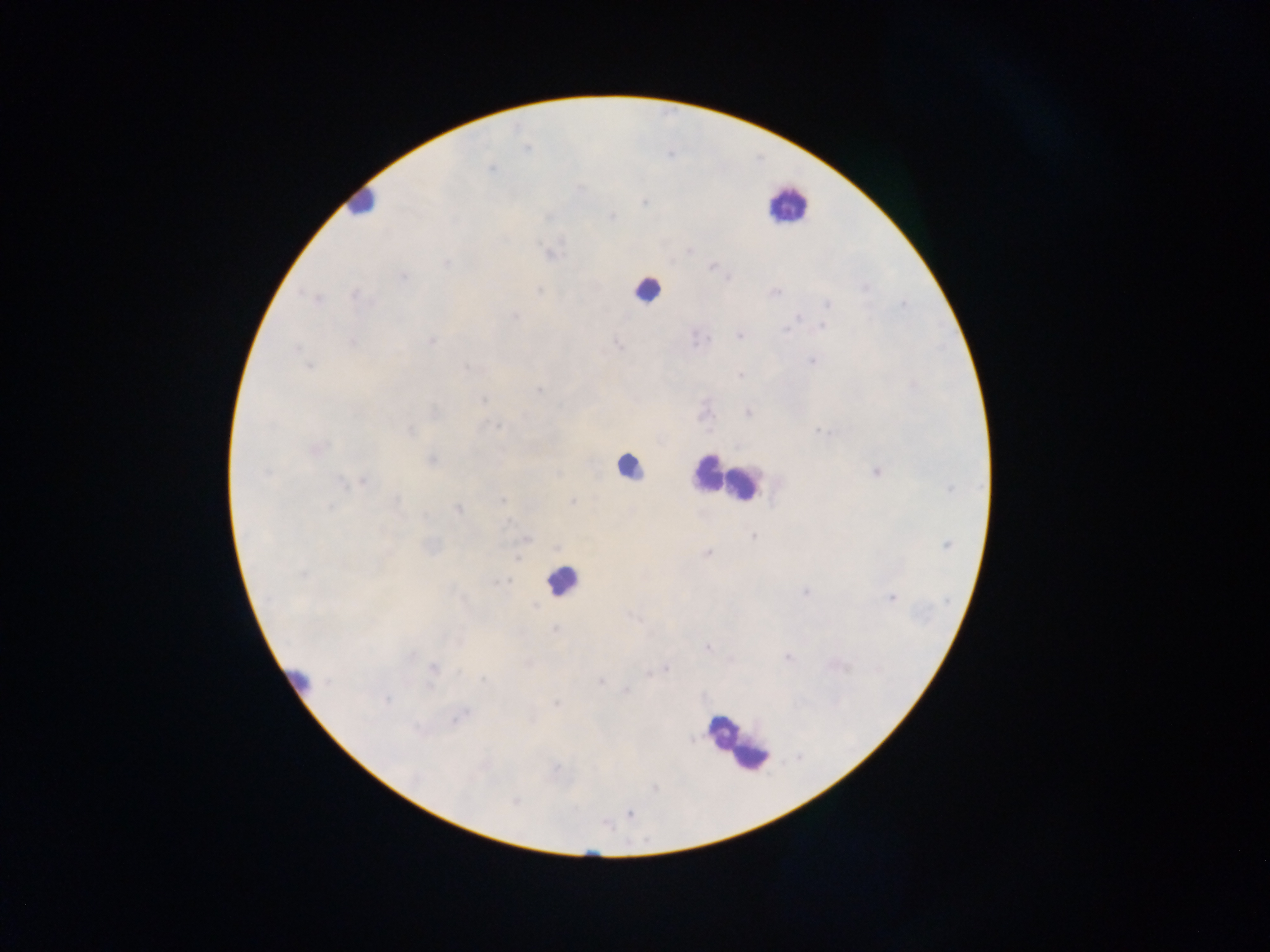
Approximate centers as [x, y] in pixels. Malaria parasite locations: [527, 149], [488, 169], [581, 187], [612, 216], [556, 248], [448, 264], [712, 267], [402, 277], [866, 288], [540, 290], [304, 292], [353, 294], [314, 298], [829, 304], [905, 305], [514, 316], [797, 318], [823, 325], [784, 329], [739, 336], [432, 341], [352, 343], [616, 343], [297, 348], [812, 361], [309, 366], [465, 367], [740, 375], [539, 389], [482, 399], [748, 412], [497, 426], [410, 430], [819, 431], [318, 449], [266, 472], [877, 473], [559, 474], [363, 481], [343, 482], [503, 500], [396, 501], [573, 501], [330, 507], [458, 509], [425, 515], [511, 523], [383, 531], [752, 536], [527, 539], [947, 544], [706, 554], [519, 557], [385, 562], [305, 575], [502, 583], [805, 592], [892, 598], [631, 616], [553, 630], [707, 647], [412, 655], [787, 657], [432, 668], [665, 670], [459, 671], [651, 674], [481, 679], [601, 681], [429, 685], [625, 691], [386, 700], [556, 703], [454, 721], [692, 740], [560, 766], [557, 770], [515, 802], [631, 814]. Leukocyte locations: [363, 201], [790, 207], [651, 293], [628, 468], [707, 472], [743, 481], [559, 577], [719, 728], [752, 755]. Image is 1270×952 pixels. One field of view. Thick blood film. Photographed through a microscope with a mobile-phone camera. Sample from Ghana.